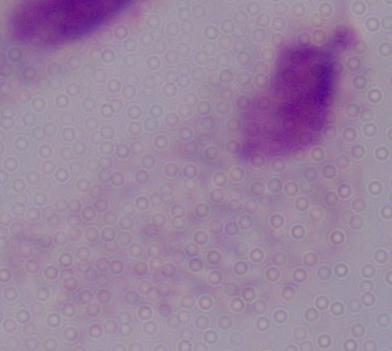 Photomicrograph. Captured at 1000x magnification. A trichomonad is shown.